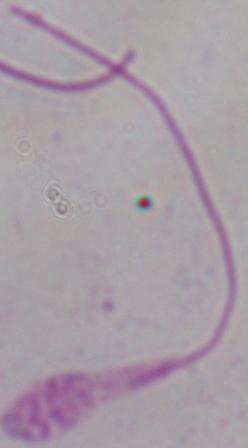 A Leishmania parasite is shown. Captured at 1000x magnification. Photomicrograph.